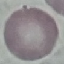

result = no malaria parasites detected
stain = Giemsa
image type = cell patch, automatically extracted from a larger field of view and resized to 64 × 64 pixels
capture = smartphone camera at the microscope eyepiece
preparation = thin blood film